State which parasite is depicted.
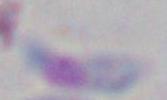

Toxoplasma gondii.

Summary:
  - Modality: photomicrograph
  - Magnification: 1000x